State which parasite is depicted.
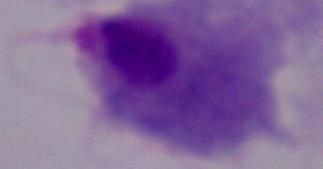
A trichomonad.

magnification = 1000x
modality = micrograph